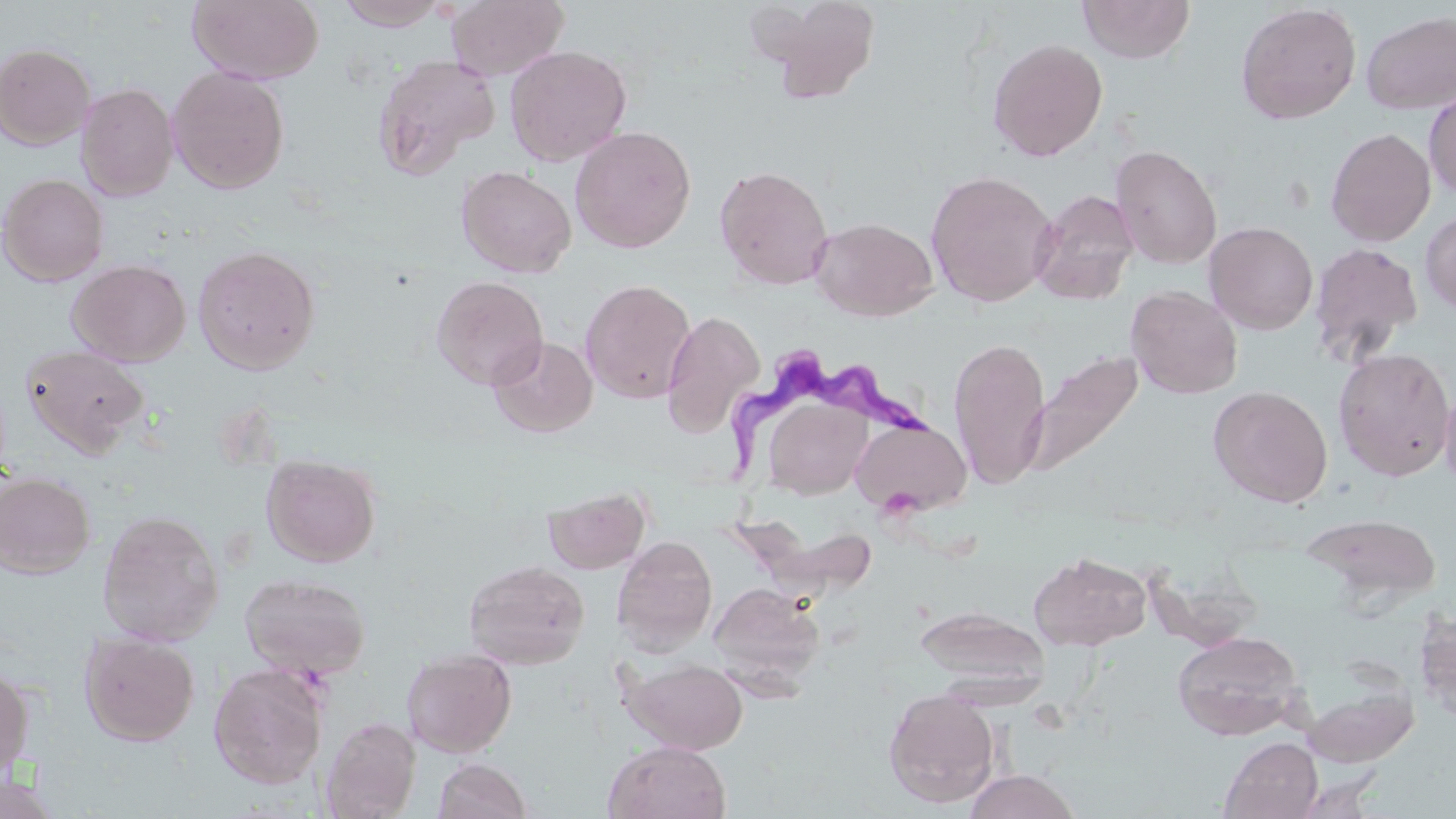

slide-level diagnosis = Trypanosoma brucei
stain = May-Grünwald-Giemsa
image size = 1456×819 pixels
uninfected red blood cell locations = approximate bounding boxes as named x1/y1/x2/y2 corners in pixels: (x1=187, y1=0, x2=324, y2=85), (x1=333, y1=0, x2=451, y2=30), (x1=446, y1=0, x2=569, y2=81), (x1=748, y1=0, x2=884, y2=103), (x1=1077, y1=0, x2=1195, y2=64), (x1=1235, y1=3, x2=1362, y2=125), (x1=1360, y1=10, x2=1456, y2=115), (x1=987, y1=38, x2=1108, y2=161), (x1=0, y1=43, x2=96, y2=150), (x1=504, y1=45, x2=631, y2=166), (x1=372, y1=53, x2=500, y2=178), (x1=167, y1=66, x2=290, y2=194), (x1=76, y1=83, x2=178, y2=201), (x1=1423, y1=85, x2=1456, y2=200), (x1=570, y1=126, x2=696, y2=253), (x1=1326, y1=127, x2=1436, y2=247), (x1=1109, y1=144, x2=1223, y2=269), (x1=456, y1=165, x2=577, y2=278), (x1=714, y1=165, x2=833, y2=290), (x1=925, y1=170, x2=1058, y2=307), (x1=0, y1=173, x2=109, y2=287), (x1=1030, y1=190, x2=1139, y2=304), (x1=1420, y1=210, x2=1456, y2=315), (x1=809, y1=217, x2=938, y2=321), (x1=1204, y1=221, x2=1318, y2=335), (x1=1308, y1=242, x2=1424, y2=366), (x1=193, y1=244, x2=321, y2=374), (x1=67, y1=258, x2=191, y2=366), (x1=431, y1=275, x2=548, y2=389), (x1=579, y1=279, x2=696, y2=404), (x1=1126, y1=285, x2=1243, y2=399), (x1=660, y1=310, x2=765, y2=437), (x1=488, y1=335, x2=598, y2=438), (x1=948, y1=337, x2=1051, y2=489), (x1=20, y1=344, x2=150, y2=458), (x1=1333, y1=348, x2=1455, y2=481), (x1=1025, y1=350, x2=1142, y2=478), (x1=1439, y1=384, x2=1456, y2=493), (x1=1208, y1=385, x2=1333, y2=507), (x1=764, y1=399, x2=874, y2=502), (x1=850, y1=417, x2=972, y2=516), (x1=262, y1=454, x2=380, y2=567), (x1=0, y1=472, x2=95, y2=579), (x1=544, y1=486, x2=651, y2=574), (x1=97, y1=509, x2=225, y2=646), (x1=1302, y1=513, x2=1442, y2=607), (x1=740, y1=514, x2=883, y2=594), (x1=612, y1=536, x2=717, y2=655), (x1=1029, y1=551, x2=1151, y2=650), (x1=463, y1=559, x2=590, y2=669), (x1=239, y1=573, x2=371, y2=680), (x1=710, y1=582, x2=825, y2=688), (x1=915, y1=604, x2=1050, y2=694), (x1=1414, y1=610, x2=1456, y2=723), (x1=79, y1=631, x2=200, y2=746), (x1=1172, y1=631, x2=1305, y2=740), (x1=402, y1=648, x2=517, y2=758), (x1=623, y1=658, x2=748, y2=754), (x1=0, y1=662, x2=34, y2=784), (x1=208, y1=663, x2=328, y2=789), (x1=1304, y1=684, x2=1419, y2=767), (x1=883, y1=688, x2=999, y2=807), (x1=321, y1=716, x2=421, y2=818), (x1=1220, y1=737, x2=1323, y2=819), (x1=604, y1=740, x2=731, y2=819), (x1=433, y1=758, x2=532, y2=818), (x1=962, y1=769, x2=1082, y2=819), (x1=1292, y1=771, x2=1385, y2=819), (x1=0, y1=772, x2=62, y2=819)
magnification = 1000x
preparation = thin blood film
modality = optical microscopy
Trypanosoma brucei locations = approximate bounding boxes as named x1/y1/x2/y2 corners in pixels: (x1=728, y1=351, x2=937, y2=478)
field of view = single